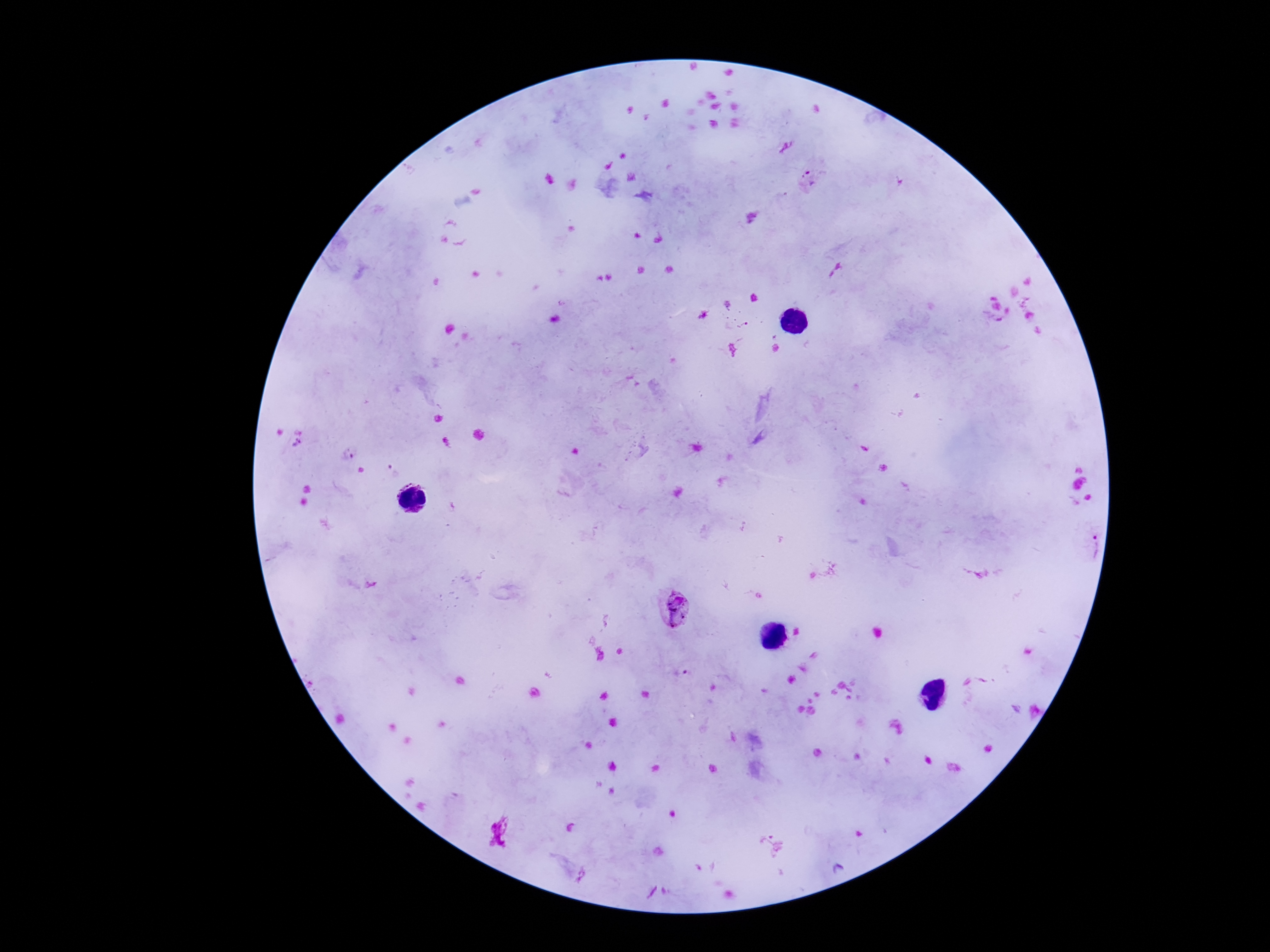
{
  "patient_malaria_status": "positive",
  "image_size": "1270×952 pixels",
  "preparation": "thick blood smear",
  "magnification": "100x",
  "plasmodium_parasite_locations": "approximate centers as {x, y} in pixels: {811, 179}, {838, 275}, {298, 443}, {348, 454}, {1079, 544}, {675, 609}, {689, 675}",
  "stain": "Giemsa",
  "field_of_view": "single",
  "capture": "smartphone camera through the microscope eyepiece"
}